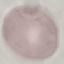

Summary:
  - Result: no malaria parasites detected
  - Capture: smartphone through the microscope eyepiece
  - Stain: Giemsa
  - Image type: automatically extracted cell patch, resized to 64 × 64 pixels
  - Preparation: thin blood smear